Report the malaria status of this cell.
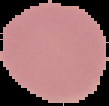

Uninfected.

From a thin blood film. Image is 109×106 pixels. The area outside the segmented cell region is set to black.